Point out each Plasmodium parasite.
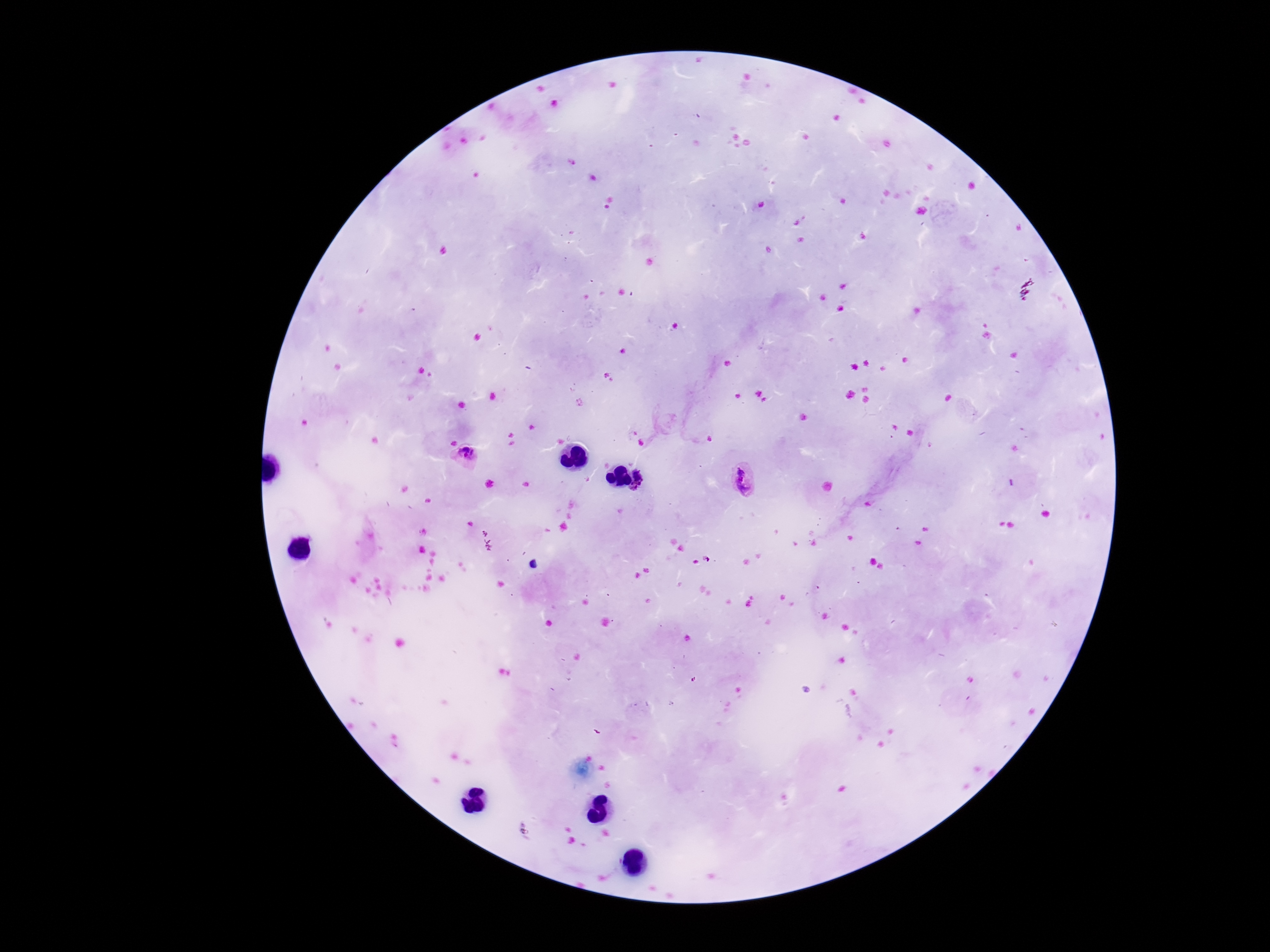
Approximate centers as [x, y] in pixels.
Plasmodium parasites: [466, 452], [637, 475], [745, 480], [634, 487].

Photographed through the microscope eyepiece with a smartphone camera. Image is 1270×952 pixels. 100x magnification. Single field of view. Giemsa-stained preparation. Patient malaria status: positive. Thick blood smear.